Assess this cell for malaria.
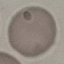

It is uninfected.

Thin smear of blood. Acquired by smartphone through the microscope eyepiece. Cell patch, automatically extracted from a larger field of view and resized to 64 × 64 pixels. Giemsa-stained preparation.